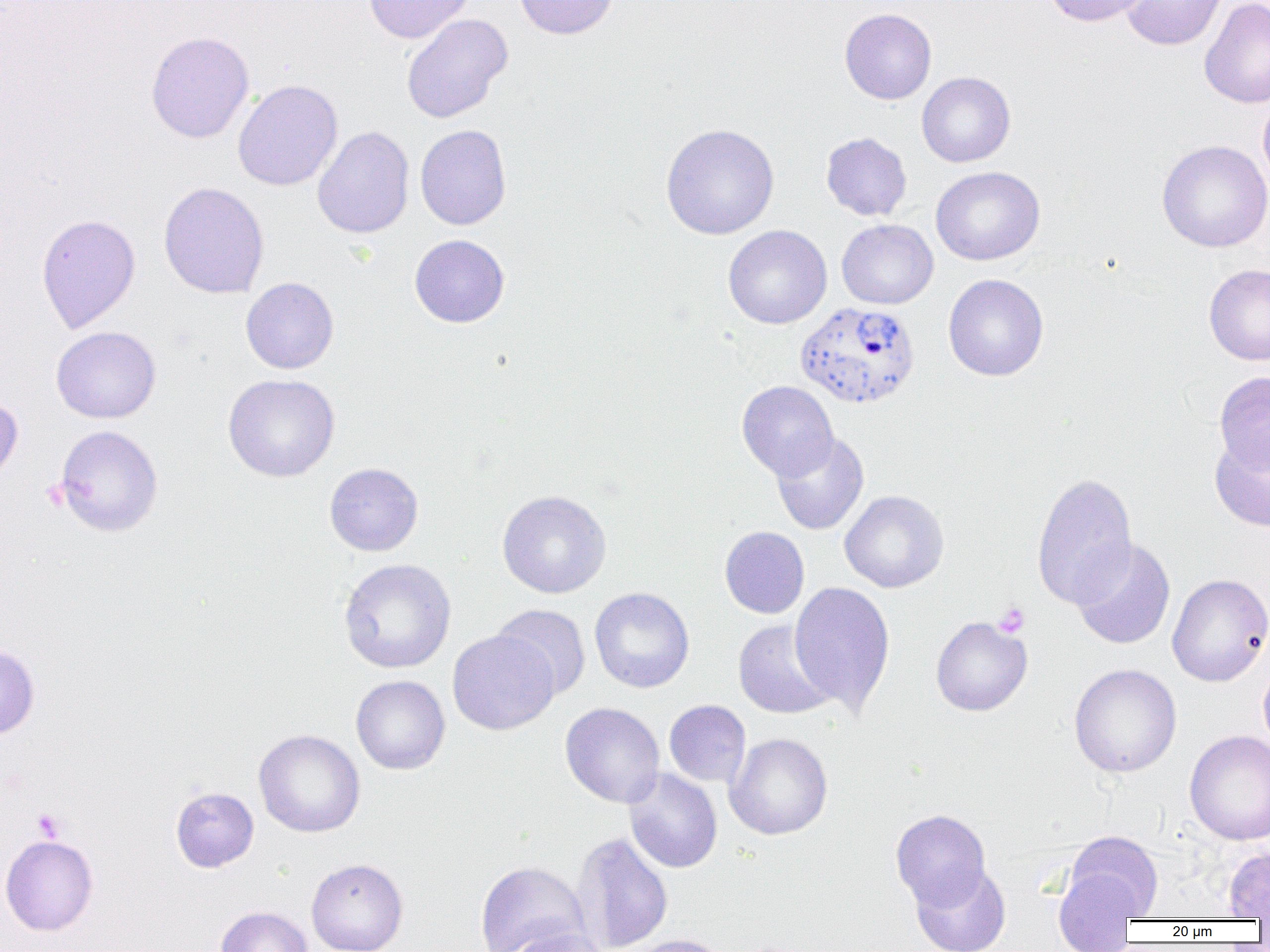
Summary:
  - Coordinate format: approximate bounding boxes as (x1, y1, x2, y2) in pixels
  - Uninfected red blood cell locations: (363, 0, 473, 44), (514, 0, 619, 40), (1044, 0, 1150, 27), (1120, 0, 1226, 51), (1199, 0, 1270, 109), (839, 8, 937, 104), (401, 13, 512, 123), (146, 30, 254, 144), (916, 72, 1015, 167), (233, 79, 343, 191), (1257, 92, 1270, 194), (660, 123, 780, 240), (415, 124, 512, 230), (312, 126, 415, 239), (821, 132, 912, 221), (1157, 140, 1270, 252), (930, 166, 1045, 265), (158, 181, 269, 299), (36, 213, 140, 333), (837, 219, 938, 309), (723, 225, 832, 329), (409, 234, 510, 328), (1204, 264, 1270, 365), (943, 274, 1049, 381), (241, 277, 339, 374), (51, 326, 161, 423), (1214, 371, 1270, 475), (223, 373, 340, 482), (737, 380, 838, 480), (0, 394, 23, 488), (54, 425, 163, 537), (771, 431, 869, 535), (1210, 433, 1270, 531), (324, 462, 424, 556), (1031, 472, 1138, 609), (497, 489, 612, 598), (839, 490, 949, 593), (719, 526, 809, 619), (1071, 538, 1175, 650), (338, 558, 456, 674), (1167, 573, 1270, 687), (789, 581, 895, 715), (590, 587, 694, 693), (491, 604, 592, 700), (931, 616, 1032, 716), (733, 620, 838, 720), (447, 629, 559, 735), (0, 644, 40, 740), (1258, 660, 1270, 753), (1069, 663, 1182, 778), (351, 675, 450, 775), (664, 700, 751, 787), (560, 702, 665, 808), (253, 729, 365, 837), (1185, 730, 1270, 846), (725, 732, 833, 840), (623, 768, 723, 873), (170, 787, 259, 872), (890, 809, 991, 910), (571, 831, 673, 952), (1064, 831, 1163, 919), (0, 834, 99, 936), (1223, 847, 1270, 919), (306, 858, 408, 952), (475, 860, 590, 952), (910, 863, 1011, 952), (1052, 867, 1140, 951), (215, 905, 314, 952), (500, 927, 612, 952), (626, 934, 731, 952)
  - Plasmodium vivax-infected red blood cell locations: (796, 302, 921, 409)
  - Platelet locations: (993, 602, 1030, 638), (33, 808, 66, 842)
  - Slide-level diagnosis: Plasmodium vivax
  - Modality: optical microscopy
  - Magnification: 1000x
  - Field of view: one of a larger specimen
  - Image size: 1270×952 pixels
  - Preparation: thin blood smear